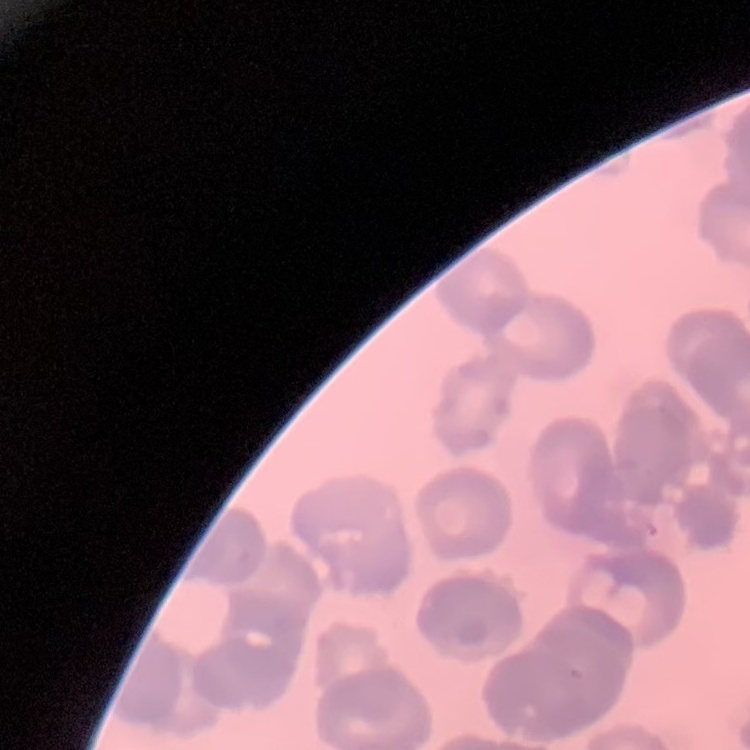

The erythrocytes exhibit rouleaux formation. Thin peripheral smear. One tile cut from a larger photomicrograph. Field's or Giemsa stain.